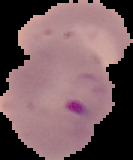
{
  "image_type": "segmented cell region with the area outside set to black",
  "preparation": "thin blood smear",
  "image_size": "133×160 pixels",
  "malaria_status": "parasitized"
}